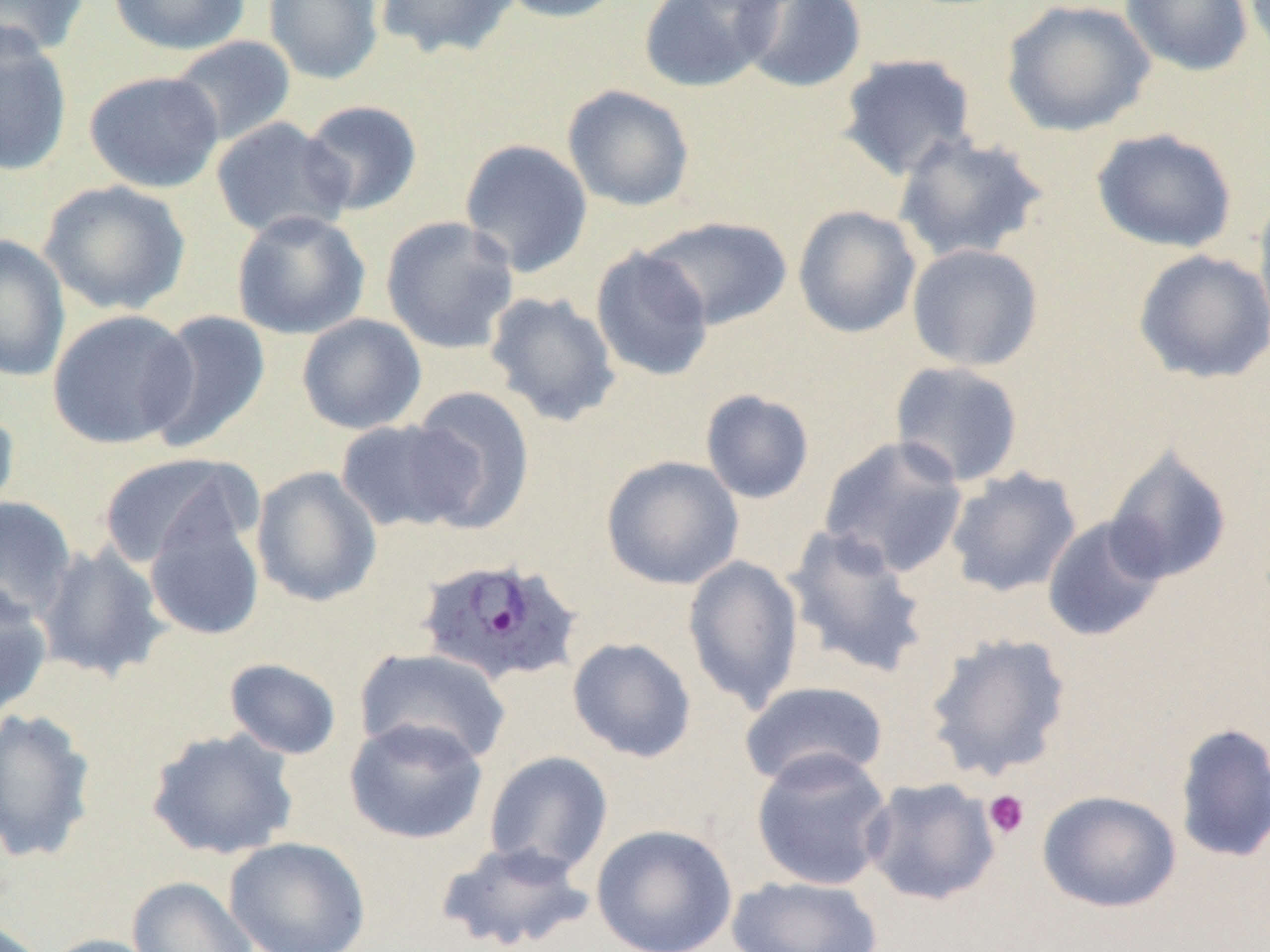 Approximate bounding boxes as named x1/y1/x2/y2 corners in pixels. Plasmodium ovale-infected red blood cell locations: (x1=414, y1=555, x2=585, y2=687). Platelet locations: (x1=983, y1=789, x2=1030, y2=839). Uninfected red blood cell locations: (x1=107, y1=0, x2=251, y2=56), (x1=263, y1=0, x2=384, y2=85), (x1=373, y1=0, x2=520, y2=59), (x1=495, y1=0, x2=630, y2=23), (x1=637, y1=0, x2=784, y2=93), (x1=735, y1=0, x2=868, y2=94), (x1=1000, y1=0, x2=1157, y2=137), (x1=1118, y1=0, x2=1254, y2=76), (x1=0, y1=1, x2=91, y2=59), (x1=0, y1=26, x2=72, y2=178), (x1=167, y1=35, x2=297, y2=147), (x1=837, y1=52, x2=978, y2=182), (x1=84, y1=70, x2=225, y2=193), (x1=562, y1=84, x2=695, y2=212), (x1=300, y1=99, x2=423, y2=216), (x1=210, y1=117, x2=354, y2=241), (x1=1090, y1=128, x2=1238, y2=253), (x1=894, y1=131, x2=1049, y2=264), (x1=459, y1=138, x2=594, y2=278), (x1=40, y1=180, x2=191, y2=315), (x1=1252, y1=190, x2=1270, y2=339), (x1=792, y1=205, x2=921, y2=339), (x1=231, y1=210, x2=371, y2=340), (x1=380, y1=215, x2=520, y2=354), (x1=642, y1=216, x2=793, y2=330), (x1=0, y1=234, x2=70, y2=382), (x1=906, y1=242, x2=1044, y2=371), (x1=591, y1=246, x2=714, y2=381), (x1=1133, y1=249, x2=1270, y2=384), (x1=484, y1=290, x2=621, y2=428), (x1=47, y1=309, x2=198, y2=449), (x1=145, y1=310, x2=272, y2=453), (x1=297, y1=313, x2=427, y2=435), (x1=889, y1=360, x2=1025, y2=488), (x1=405, y1=387, x2=536, y2=532), (x1=700, y1=389, x2=815, y2=504), (x1=0, y1=403, x2=20, y2=524), (x1=334, y1=419, x2=476, y2=534), (x1=817, y1=435, x2=970, y2=579), (x1=1104, y1=446, x2=1233, y2=585), (x1=97, y1=452, x2=257, y2=570), (x1=601, y1=455, x2=744, y2=590), (x1=251, y1=466, x2=382, y2=607), (x1=945, y1=467, x2=1082, y2=599), (x1=0, y1=496, x2=77, y2=624), (x1=143, y1=509, x2=266, y2=642), (x1=1042, y1=516, x2=1168, y2=642), (x1=782, y1=524, x2=932, y2=680), (x1=34, y1=544, x2=170, y2=682), (x1=682, y1=554, x2=805, y2=714), (x1=0, y1=583, x2=53, y2=721), (x1=923, y1=631, x2=1073, y2=783), (x1=567, y1=637, x2=697, y2=763), (x1=355, y1=647, x2=512, y2=767), (x1=224, y1=658, x2=342, y2=760), (x1=739, y1=680, x2=890, y2=789), (x1=0, y1=707, x2=98, y2=865), (x1=344, y1=717, x2=488, y2=845), (x1=1172, y1=722, x2=1270, y2=863), (x1=146, y1=727, x2=300, y2=861), (x1=749, y1=748, x2=895, y2=891), (x1=484, y1=750, x2=613, y2=877), (x1=861, y1=777, x2=1001, y2=907), (x1=1037, y1=789, x2=1182, y2=913), (x1=590, y1=823, x2=738, y2=952), (x1=224, y1=836, x2=371, y2=952), (x1=434, y1=839, x2=596, y2=952), (x1=725, y1=875, x2=884, y2=952), (x1=127, y1=876, x2=258, y2=952), (x1=39, y1=934, x2=167, y2=952). Slide-level diagnosis: Plasmodium ovale. Single field of view. Thin blood smear. 1000x magnification. Light microscopy. Image is 1270×952 pixels.